Classify this cell by malaria status.
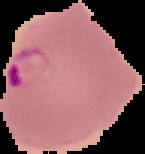

Parasitized.

Summary:
  - Image type: segmented cell region with the area outside set to black
  - Image size: 145×154 pixels
  - Preparation: thin blood smear